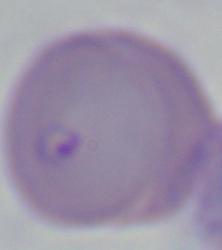
magnification = 1000x
modality = photomicrograph
identification = Babesia